Name the blood parasite species.
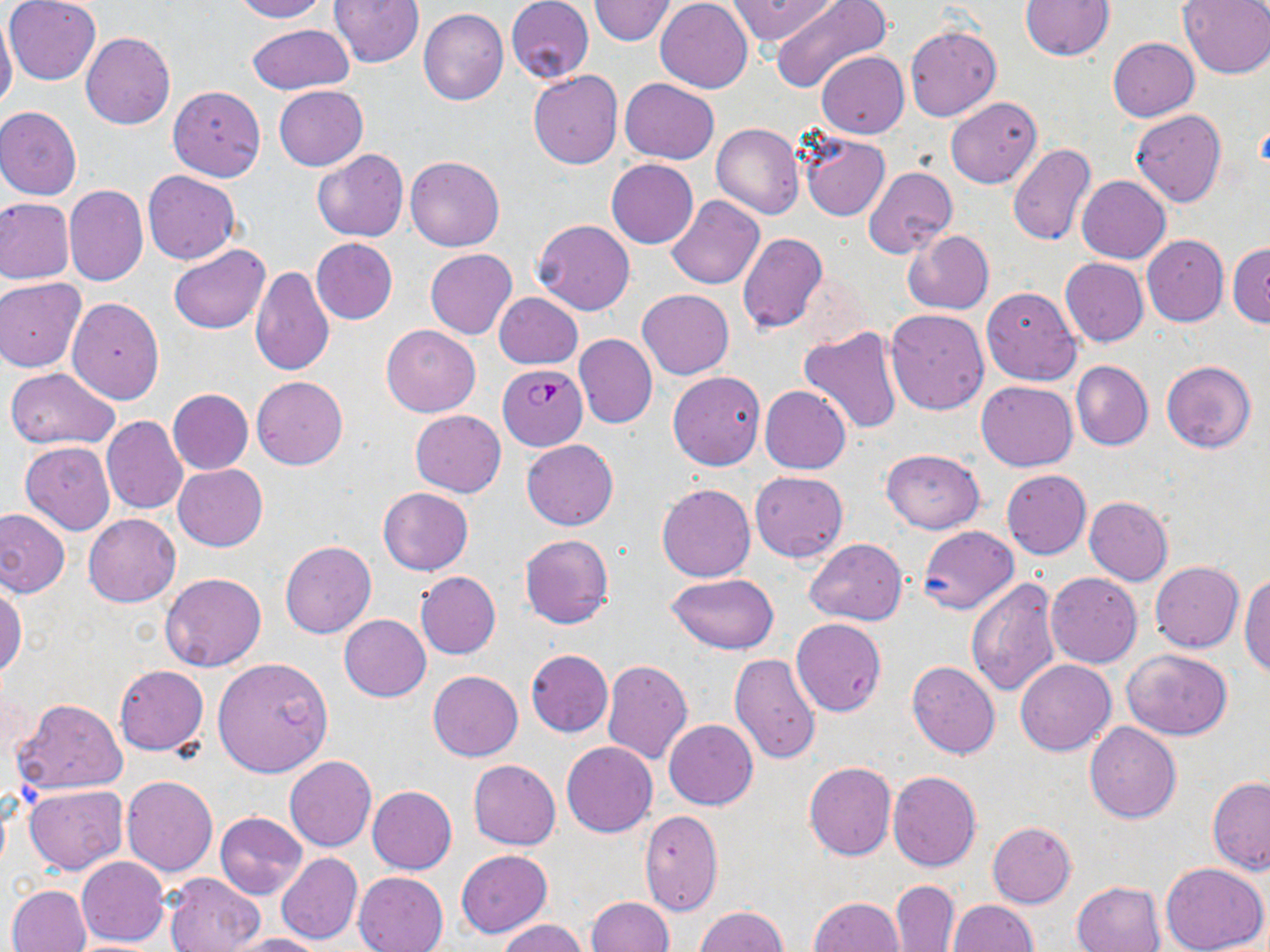

Plasmodium falciparum.

modality: light microscopy
magnification: 1000x
uninfected_red_blood_cell_locations: 'approximate bounding boxes as (x1, y1, x2, y2) in pixels: (230, 0, 327, 21), (329, 0, 424, 68), (588, 0, 675, 45), (655, 0, 752, 92), (726, 0, 838, 46), (772, 0, 894, 98), (1177, 0, 1270, 78), (3, 1, 101, 85), (505, 1, 594, 83), (1021, 1, 1115, 60), (419, 9, 509, 106), (0, 12, 18, 115), (246, 24, 353, 95), (905, 26, 1002, 123), (80, 32, 175, 129), (1108, 37, 1199, 121), (816, 52, 909, 139), (528, 71, 623, 169), (620, 78, 719, 164), (168, 84, 266, 181), (274, 85, 367, 170), (945, 96, 1042, 188), (0, 107, 81, 200), (1129, 109, 1228, 208), (713, 123, 804, 219), (800, 133, 889, 221), (1007, 143, 1096, 247), (312, 148, 408, 242), (404, 155, 505, 251), (606, 159, 698, 248), (863, 166, 956, 257), (143, 171, 240, 264), (1077, 175, 1171, 262), (64, 185, 148, 286), (666, 194, 765, 289), (0, 199, 75, 284), (531, 219, 635, 314), (903, 229, 995, 314), (738, 232, 828, 334), (1142, 235, 1228, 327), (311, 238, 397, 324), (1227, 242, 1270, 328), (168, 244, 270, 334), (424, 249, 517, 338), (1060, 257, 1149, 346), (250, 266, 334, 377), (792, 270, 871, 351), (1, 277, 86, 372), (982, 287, 1081, 385), (638, 289, 733, 379), (494, 292, 582, 369), (68, 297, 164, 404), (885, 307, 989, 415), (381, 324, 481, 417), (797, 326, 904, 434), (573, 333, 657, 428), (1071, 360, 1153, 451), (1162, 361, 1257, 454), (5, 367, 119, 450), (668, 371, 765, 470), (252, 376, 347, 470), (975, 380, 1078, 470), (760, 385, 851, 474), (167, 389, 252, 475), (410, 410, 505, 497), (102, 415, 188, 513), (522, 440, 617, 530), (20, 441, 115, 534), (881, 449, 984, 533), (173, 464, 267, 550), (1001, 469, 1091, 559), (750, 470, 848, 563), (657, 482, 755, 582), (378, 488, 472, 576), (1084, 496, 1173, 584), (0, 507, 70, 597), (84, 514, 180, 607), (917, 526, 1020, 614), (519, 533, 614, 630), (804, 539, 907, 625), (280, 541, 376, 638), (1150, 562, 1244, 653), (415, 571, 501, 659), (161, 572, 267, 671), (1046, 572, 1141, 668), (668, 573, 780, 653), (1239, 573, 1269, 678), (964, 576, 1060, 698), (0, 579, 26, 677), (339, 614, 431, 701), (791, 617, 887, 716), (1123, 649, 1233, 740), (525, 650, 613, 737), (729, 653, 821, 765), (212, 657, 333, 776), (1015, 659, 1117, 756), (601, 660, 693, 763), (908, 661, 1000, 758), (115, 665, 208, 755), (429, 670, 523, 761), (13, 697, 128, 794), (664, 719, 758, 810), (1084, 722, 1182, 823), (561, 742, 657, 837), (284, 756, 376, 852), (469, 760, 561, 850), (804, 761, 897, 861), (887, 770, 981, 871), (121, 775, 218, 877), (1208, 776, 1270, 872), (1193, 777, 1267, 948), (23, 783, 127, 874), (368, 786, 457, 874), (639, 810, 724, 916), (215, 812, 307, 899), (987, 822, 1076, 908), (456, 849, 553, 937), (276, 853, 363, 945), (77, 856, 168, 947), (1161, 863, 1269, 952), (353, 871, 448, 952), (162, 872, 264, 952), (889, 880, 959, 951), (1072, 881, 1166, 952), (7, 884, 92, 952), (809, 896, 901, 951), (586, 897, 674, 952), (948, 900, 1037, 951), (694, 906, 787, 951), (497, 919, 587, 952), (225, 933, 326, 952), (60, 939, 170, 951)'
preparation: thin blood film
stain: May-Grünwald-Giemsa
image_size: 1270×952 pixels
plasmodium_falciparum_infected_red_blood_cell_locations: 'approximate bounding boxes as (x1, y1, x2, y2) in pixels: (499, 363, 588, 450)'
field_of_view: one of a larger specimen